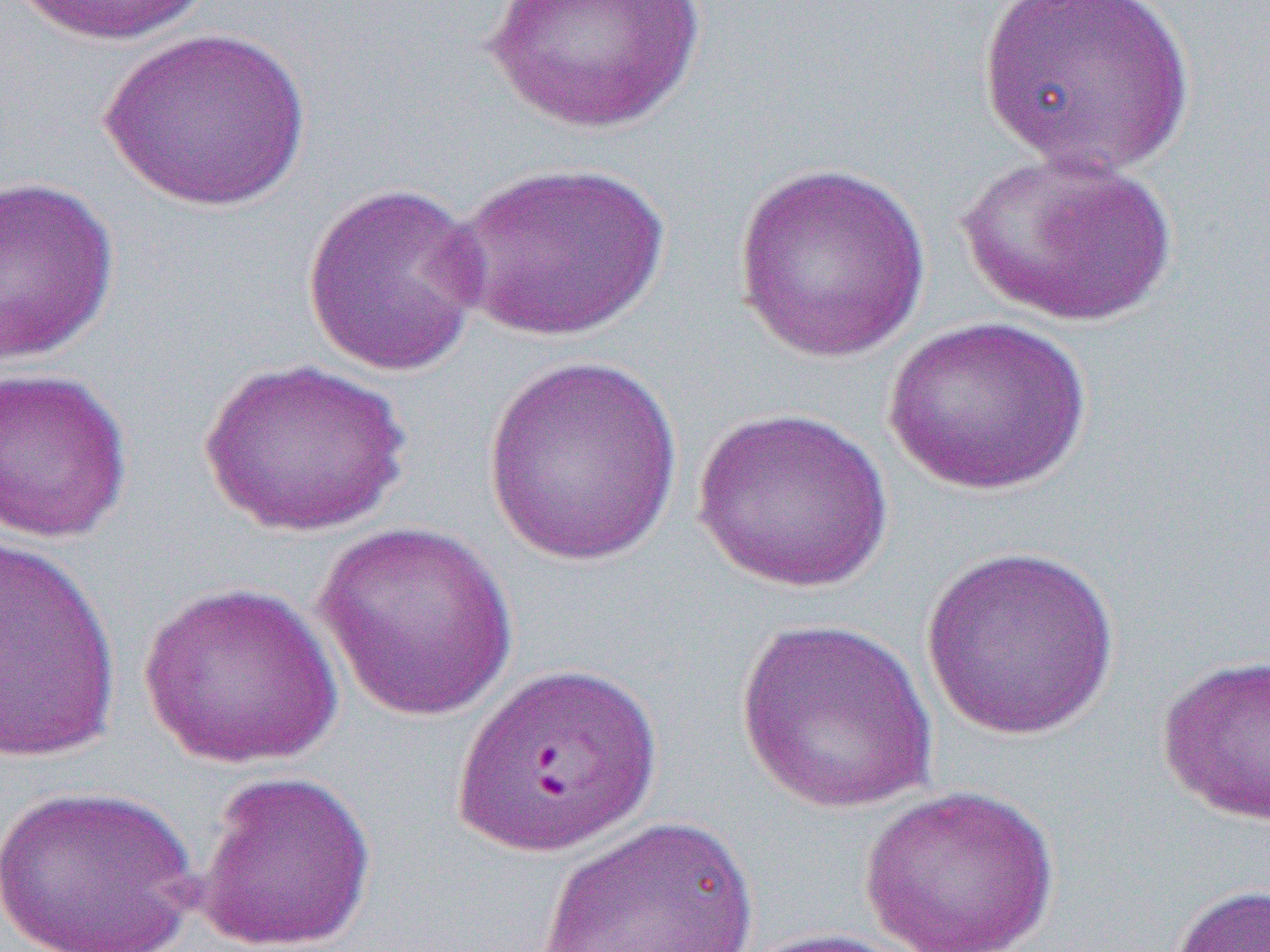

Summary:
  - Coordinate format: approximate bounding boxes as (x1,y1)-(x2,y2) corner pairs in pixels
  - Uninfected red blood cell locations: (4,0)-(215,47), (479,0)-(708,137), (978,0)-(1197,179), (101,27)-(312,212), (956,149)-(1178,327), (451,160)-(673,342), (733,163)-(932,363), (0,174)-(121,366), (300,181)-(492,378), (881,315)-(1094,497), (480,353)-(684,568), (198,357)-(411,538), (0,367)-(135,544), (694,406)-(893,592), (313,521)-(522,721), (0,534)-(122,765), (920,546)-(1122,740), (138,580)-(342,770), (734,616)-(939,814), (1155,653)-(1270,825), (194,769)-(378,952), (2,783)-(203,951), (859,784)-(1059,951), (535,815)-(762,952), (1164,883)-(1270,952), (739,927)-(925,952)
  - Slide-level diagnosis: Plasmodium falciparum
  - Magnification: 1000x
  - Image size: 1270×952 pixels
  - Preparation: thin blood smear
  - Field of view: single
  - Modality: light microscopy